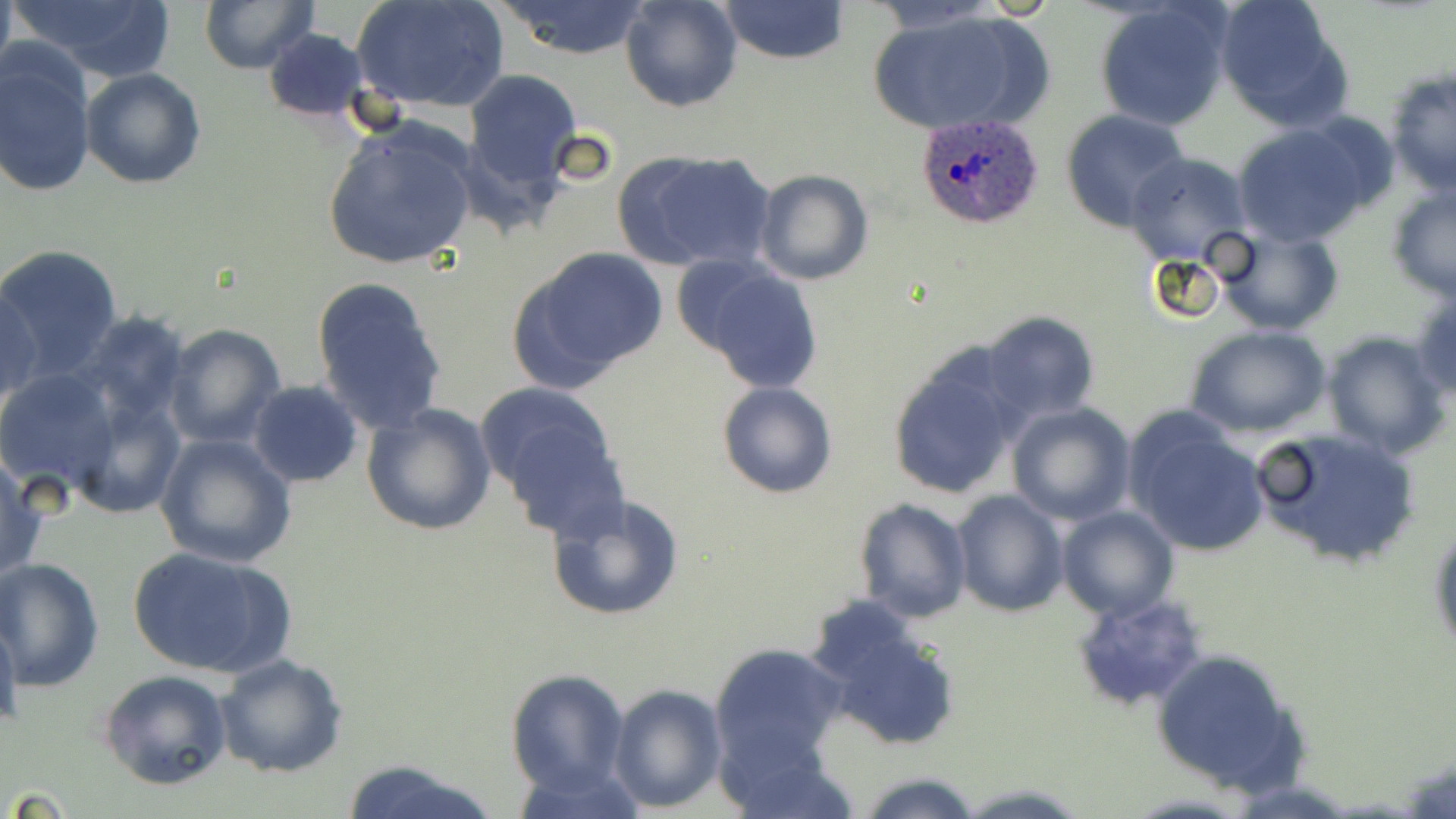
Summary:
  - Coordinate format: approximate bounding boxes as named x1/y1/x2/y2 corners in pixels
  - Uninfected red blood cell locations: (x1=9, y1=0, x2=179, y2=83), (x1=198, y1=0, x2=318, y2=74), (x1=352, y1=0, x2=511, y2=115), (x1=619, y1=0, x2=742, y2=113), (x1=719, y1=0, x2=849, y2=64), (x1=1215, y1=0, x2=1352, y2=130), (x1=493, y1=1, x2=654, y2=61), (x1=1093, y1=3, x2=1232, y2=133), (x1=868, y1=9, x2=1038, y2=136), (x1=262, y1=28, x2=372, y2=123), (x1=0, y1=44, x2=97, y2=199), (x1=1385, y1=67, x2=1455, y2=196), (x1=80, y1=68, x2=206, y2=189), (x1=462, y1=69, x2=583, y2=190), (x1=1060, y1=109, x2=1191, y2=232), (x1=321, y1=120, x2=480, y2=273), (x1=1230, y1=125, x2=1371, y2=246), (x1=625, y1=150, x2=776, y2=273), (x1=1125, y1=152, x2=1252, y2=266), (x1=751, y1=169, x2=875, y2=286), (x1=1386, y1=183, x2=1456, y2=303), (x1=1216, y1=225, x2=1345, y2=335), (x1=0, y1=245, x2=121, y2=379), (x1=513, y1=247, x2=666, y2=389), (x1=686, y1=265, x2=827, y2=395), (x1=311, y1=277, x2=448, y2=437), (x1=1, y1=282, x2=41, y2=410), (x1=1408, y1=285, x2=1456, y2=406), (x1=978, y1=310, x2=1101, y2=427), (x1=71, y1=312, x2=192, y2=430), (x1=163, y1=322, x2=286, y2=449), (x1=1187, y1=325, x2=1329, y2=438), (x1=1322, y1=331, x2=1450, y2=458), (x1=885, y1=350, x2=1023, y2=501), (x1=0, y1=370, x2=121, y2=495), (x1=248, y1=381, x2=364, y2=486), (x1=717, y1=381, x2=837, y2=499), (x1=477, y1=385, x2=624, y2=529), (x1=66, y1=390, x2=186, y2=522), (x1=359, y1=401, x2=498, y2=538), (x1=1006, y1=402, x2=1137, y2=525), (x1=1124, y1=414, x2=1271, y2=558), (x1=1252, y1=424, x2=1423, y2=569), (x1=155, y1=435, x2=298, y2=572), (x1=0, y1=451, x2=47, y2=584), (x1=951, y1=490, x2=1069, y2=617), (x1=546, y1=493, x2=685, y2=622), (x1=856, y1=498, x2=972, y2=624), (x1=1056, y1=505, x2=1178, y2=620), (x1=1429, y1=517, x2=1456, y2=661), (x1=126, y1=546, x2=292, y2=681), (x1=0, y1=558, x2=104, y2=691), (x1=1072, y1=592, x2=1210, y2=713), (x1=812, y1=604, x2=962, y2=752), (x1=0, y1=609, x2=21, y2=738), (x1=710, y1=641, x2=849, y2=774), (x1=1148, y1=647, x2=1311, y2=796), (x1=215, y1=654, x2=348, y2=777), (x1=504, y1=668, x2=631, y2=796), (x1=100, y1=670, x2=235, y2=792), (x1=608, y1=683, x2=726, y2=812), (x1=335, y1=760, x2=498, y2=819), (x1=858, y1=772, x2=984, y2=818), (x1=954, y1=781, x2=1091, y2=819)
  - Plasmodium ovale-infected red blood cell locations: (x1=913, y1=114, x2=1046, y2=229)
  - Slide-level diagnosis: Plasmodium ovale
  - Field of view: one of a larger specimen
  - Image size: 1456×819 pixels
  - Magnification: 1000x
  - Stain: May-Grünwald-Giemsa
  - Modality: light microscopy
  - Preparation: thin blood smear